Give the extent of all Plasmodium falciparum-infected red blood cells.
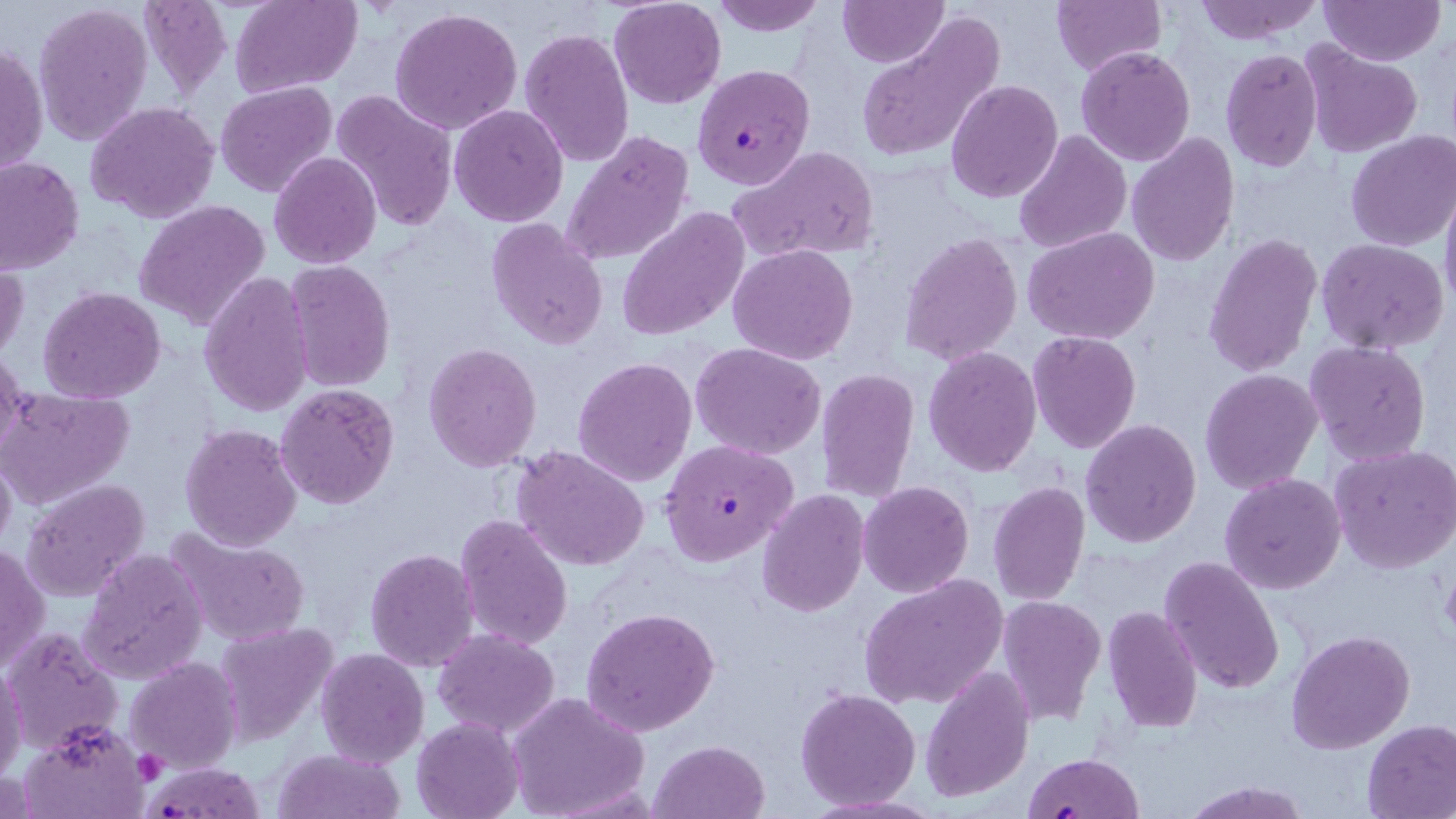
Approximate bounding boxes as [x1, y1, x2, y2] in pixels.
Plasmodium falciparum-infected red blood cells: [692, 64, 813, 190], [660, 439, 798, 567], [1020, 751, 1142, 818], [147, 760, 265, 816].

slide-level diagnosis = Plasmodium falciparum
platelet locations = approximate bounding boxes as [x1, y1, x2, y2] in pixels: [1439, 568, 1456, 641], [136, 750, 168, 783]
magnification = 1000x
uninfected red blood cell locations = approximate bounding boxes as [x1, y1, x2, y2] in pixels: [137, 0, 233, 100], [229, 0, 362, 96], [608, 0, 726, 110], [710, 0, 827, 35], [838, 0, 946, 67], [1049, 0, 1165, 76], [1191, 0, 1324, 45], [1320, 0, 1444, 65], [34, 3, 154, 148], [390, 6, 524, 136], [1314, 8, 1436, 122], [853, 12, 1006, 163], [519, 27, 634, 167], [1, 43, 48, 180], [1300, 44, 1424, 159], [1075, 46, 1196, 166], [1219, 47, 1323, 173], [946, 79, 1063, 203], [215, 81, 338, 199], [330, 90, 460, 231], [86, 100, 220, 223], [448, 104, 568, 227], [1013, 130, 1131, 253], [560, 131, 695, 268], [1346, 131, 1456, 251], [1125, 133, 1239, 267], [729, 144, 883, 263], [268, 151, 381, 270], [0, 158, 84, 274], [1441, 182, 1456, 311], [136, 200, 270, 330], [615, 208, 748, 340], [486, 218, 609, 350], [1023, 227, 1160, 346], [899, 232, 1022, 367], [1203, 233, 1323, 377], [1316, 237, 1449, 354], [728, 244, 859, 365], [284, 259, 396, 392], [1, 260, 27, 365], [200, 271, 313, 417], [37, 287, 167, 404], [1027, 332, 1142, 455], [1305, 339, 1434, 466], [424, 342, 542, 470], [690, 343, 827, 459], [923, 346, 1042, 476], [0, 347, 27, 458], [573, 356, 696, 486], [816, 368, 920, 500], [1200, 369, 1323, 494], [274, 383, 401, 510], [0, 387, 134, 510], [1079, 419, 1202, 548], [180, 422, 304, 552], [0, 443, 16, 557], [1328, 444, 1456, 573], [511, 445, 652, 572], [1220, 473, 1346, 593], [22, 479, 150, 602], [859, 481, 973, 598], [989, 481, 1091, 606], [756, 489, 869, 616], [455, 513, 575, 651], [168, 528, 313, 647], [0, 542, 48, 676], [79, 547, 207, 685], [364, 547, 480, 673], [1159, 554, 1285, 696], [859, 573, 1008, 709], [994, 595, 1106, 726], [581, 605, 719, 737], [1103, 606, 1203, 732], [212, 622, 336, 745], [2, 627, 121, 755], [1286, 629, 1414, 755], [431, 630, 560, 737], [315, 647, 428, 767], [126, 659, 242, 773], [0, 662, 27, 788], [920, 667, 1034, 801], [795, 687, 923, 810], [505, 692, 650, 819], [411, 717, 524, 819], [17, 719, 150, 818], [1362, 719, 1456, 818], [649, 740, 769, 819], [272, 747, 404, 819], [1180, 778, 1312, 819]
preparation = thin blood smear
modality = optical microscopy
stain = May-Grünwald-Giemsa
image size = 1456×819 pixels
field of view = single